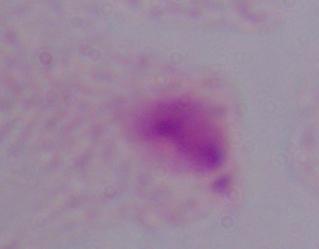

magnification: 1000x
modality: micrograph
identification: trichomonad